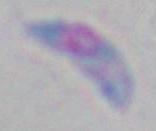
modality = photomicrograph
magnification = 1000x
identification = Toxoplasma gondii